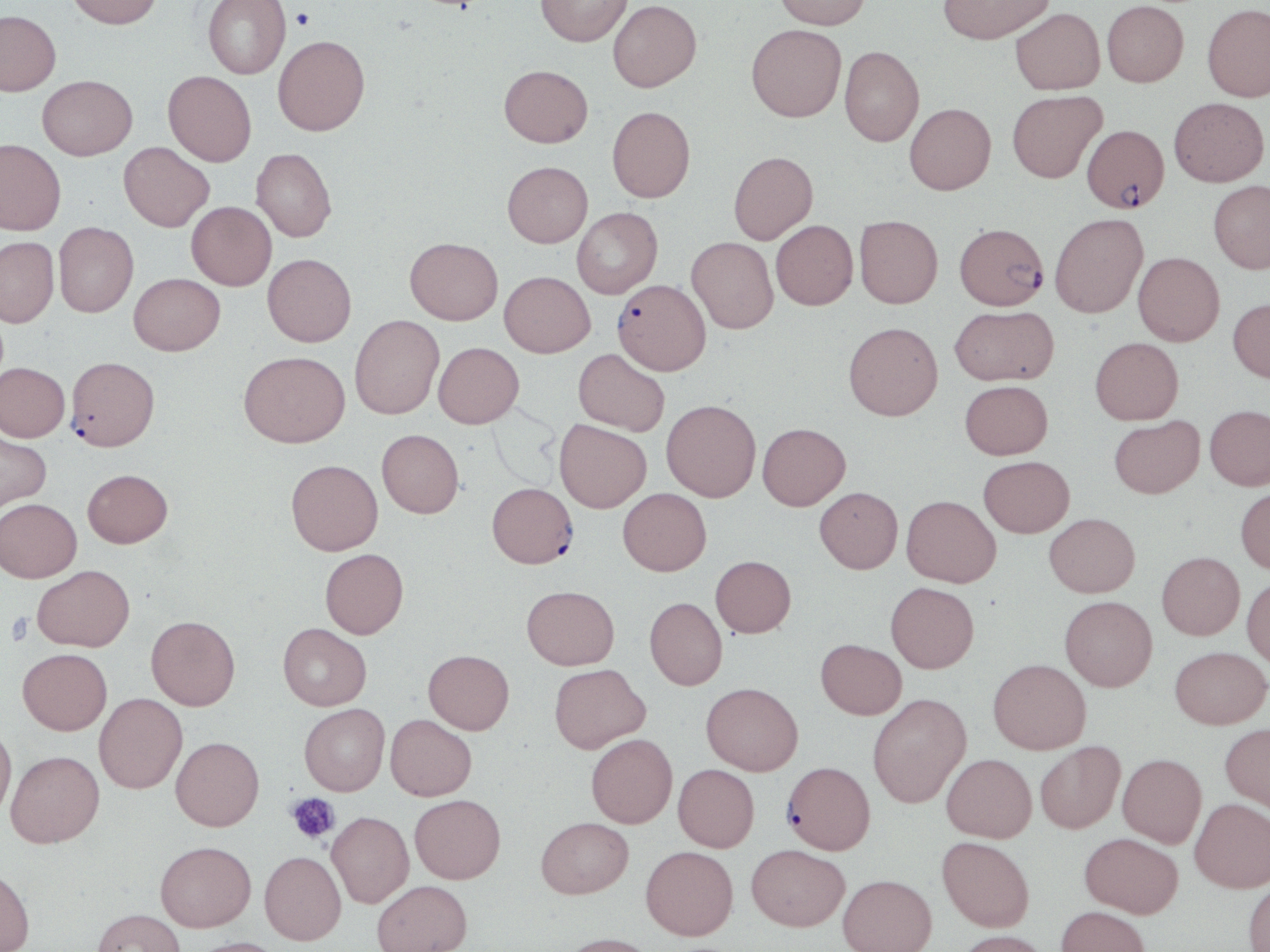
slide-level diagnosis = Plasmodium falciparum
platelet locations = approximate bounding boxes as named x1/y1/x2/y2 corners in pixels: (x1=290, y1=7, x2=315, y2=31), (x1=5, y1=612, x2=33, y2=645), (x1=287, y1=793, x2=339, y2=843)
modality = light microscopy
magnification = 1000x
field of view = single
stain = May-Grünwald-Giemsa
Plasmodium falciparum-infected red blood cell locations = approximate bounding boxes as named x1/y1/x2/y2 corners in pixels: (x1=1082, y1=124, x2=1169, y2=213), (x1=954, y1=222, x2=1048, y2=309), (x1=613, y1=279, x2=710, y2=375), (x1=65, y1=356, x2=160, y2=451), (x1=487, y1=482, x2=578, y2=568), (x1=782, y1=761, x2=876, y2=854)
image size = 1270×952 pixels
preparation = thin blood smear
uninfected red blood cell locations = approximate bounding boxes as named x1/y1/x2/y2 corners in pixels: (x1=67, y1=0, x2=163, y2=29), (x1=202, y1=0, x2=291, y2=79), (x1=535, y1=0, x2=632, y2=47), (x1=608, y1=0, x2=701, y2=92), (x1=774, y1=0, x2=871, y2=29), (x1=938, y1=0, x2=1054, y2=44), (x1=1102, y1=0, x2=1188, y2=87), (x1=1202, y1=3, x2=1270, y2=102), (x1=1010, y1=8, x2=1105, y2=94), (x1=0, y1=10, x2=61, y2=96), (x1=746, y1=24, x2=846, y2=122), (x1=273, y1=35, x2=370, y2=135), (x1=839, y1=46, x2=924, y2=146), (x1=499, y1=65, x2=593, y2=147), (x1=163, y1=70, x2=257, y2=166), (x1=38, y1=75, x2=137, y2=160), (x1=1007, y1=90, x2=1107, y2=183), (x1=1169, y1=97, x2=1269, y2=187), (x1=905, y1=103, x2=996, y2=194), (x1=607, y1=106, x2=695, y2=202), (x1=0, y1=139, x2=65, y2=235), (x1=119, y1=142, x2=214, y2=231), (x1=251, y1=148, x2=336, y2=242), (x1=728, y1=151, x2=818, y2=244), (x1=502, y1=161, x2=593, y2=247), (x1=1208, y1=180, x2=1270, y2=273), (x1=187, y1=201, x2=276, y2=290), (x1=572, y1=207, x2=662, y2=298), (x1=1050, y1=212, x2=1148, y2=318), (x1=854, y1=215, x2=943, y2=308), (x1=771, y1=220, x2=858, y2=309), (x1=53, y1=222, x2=138, y2=317), (x1=0, y1=237, x2=59, y2=328), (x1=405, y1=237, x2=503, y2=325), (x1=687, y1=237, x2=778, y2=333), (x1=1133, y1=252, x2=1225, y2=345), (x1=262, y1=253, x2=357, y2=346), (x1=499, y1=271, x2=595, y2=357), (x1=129, y1=272, x2=225, y2=355), (x1=1228, y1=298, x2=1270, y2=382), (x1=949, y1=305, x2=1059, y2=385), (x1=349, y1=315, x2=444, y2=419), (x1=843, y1=322, x2=942, y2=420), (x1=1090, y1=337, x2=1183, y2=424), (x1=433, y1=342, x2=523, y2=428), (x1=573, y1=348, x2=670, y2=435), (x1=239, y1=350, x2=350, y2=447), (x1=0, y1=362, x2=69, y2=442), (x1=960, y1=379, x2=1053, y2=459), (x1=662, y1=399, x2=761, y2=501), (x1=1205, y1=405, x2=1270, y2=490), (x1=1109, y1=416, x2=1204, y2=498), (x1=555, y1=419, x2=652, y2=512), (x1=757, y1=422, x2=851, y2=510), (x1=377, y1=429, x2=464, y2=518), (x1=0, y1=430, x2=51, y2=514), (x1=978, y1=455, x2=1075, y2=537), (x1=286, y1=459, x2=383, y2=555), (x1=83, y1=469, x2=173, y2=547), (x1=815, y1=486, x2=903, y2=573), (x1=1236, y1=487, x2=1270, y2=574), (x1=618, y1=488, x2=711, y2=575), (x1=901, y1=494, x2=1001, y2=587), (x1=0, y1=498, x2=81, y2=582), (x1=1044, y1=512, x2=1140, y2=597), (x1=320, y1=548, x2=408, y2=638), (x1=1157, y1=551, x2=1244, y2=639), (x1=710, y1=555, x2=796, y2=637), (x1=32, y1=564, x2=134, y2=651), (x1=1242, y1=577, x2=1270, y2=668), (x1=886, y1=582, x2=979, y2=672), (x1=522, y1=585, x2=619, y2=669), (x1=1060, y1=595, x2=1157, y2=691), (x1=645, y1=597, x2=727, y2=689), (x1=146, y1=615, x2=240, y2=711), (x1=278, y1=623, x2=371, y2=710), (x1=816, y1=638, x2=907, y2=719), (x1=1170, y1=646, x2=1269, y2=729), (x1=18, y1=648, x2=112, y2=735), (x1=423, y1=650, x2=514, y2=734), (x1=988, y1=658, x2=1090, y2=753), (x1=549, y1=663, x2=649, y2=753), (x1=702, y1=682, x2=803, y2=775), (x1=867, y1=692, x2=972, y2=808), (x1=94, y1=693, x2=187, y2=793), (x1=299, y1=703, x2=390, y2=795), (x1=385, y1=714, x2=476, y2=800), (x1=1220, y1=723, x2=1270, y2=815), (x1=0, y1=724, x2=16, y2=820), (x1=586, y1=733, x2=677, y2=827), (x1=171, y1=736, x2=264, y2=830), (x1=1035, y1=740, x2=1125, y2=833), (x1=6, y1=750, x2=104, y2=848), (x1=941, y1=753, x2=1036, y2=842), (x1=1117, y1=753, x2=1207, y2=847), (x1=673, y1=764, x2=759, y2=852), (x1=410, y1=794, x2=505, y2=883), (x1=1190, y1=798, x2=1270, y2=892), (x1=327, y1=811, x2=414, y2=908), (x1=536, y1=817, x2=633, y2=898), (x1=1079, y1=832, x2=1184, y2=917), (x1=937, y1=836, x2=1035, y2=931), (x1=155, y1=840, x2=256, y2=931), (x1=746, y1=844, x2=850, y2=930), (x1=641, y1=846, x2=738, y2=940), (x1=259, y1=851, x2=346, y2=944), (x1=0, y1=866, x2=35, y2=952), (x1=838, y1=873, x2=937, y2=952), (x1=1243, y1=878, x2=1270, y2=952), (x1=372, y1=880, x2=472, y2=952), (x1=1056, y1=905, x2=1151, y2=952), (x1=91, y1=908, x2=185, y2=952), (x1=955, y1=930, x2=1052, y2=952), (x1=559, y1=933, x2=660, y2=952), (x1=186, y1=936, x2=287, y2=952)